Name the parasite shown.
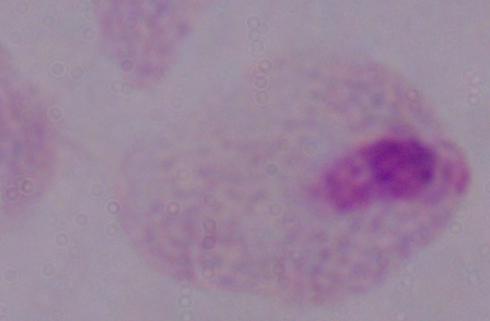
A trichomonad.

Summary:
  - Modality: micrograph
  - Magnification: 1000x